Give the position of every Plasmodium parasite.
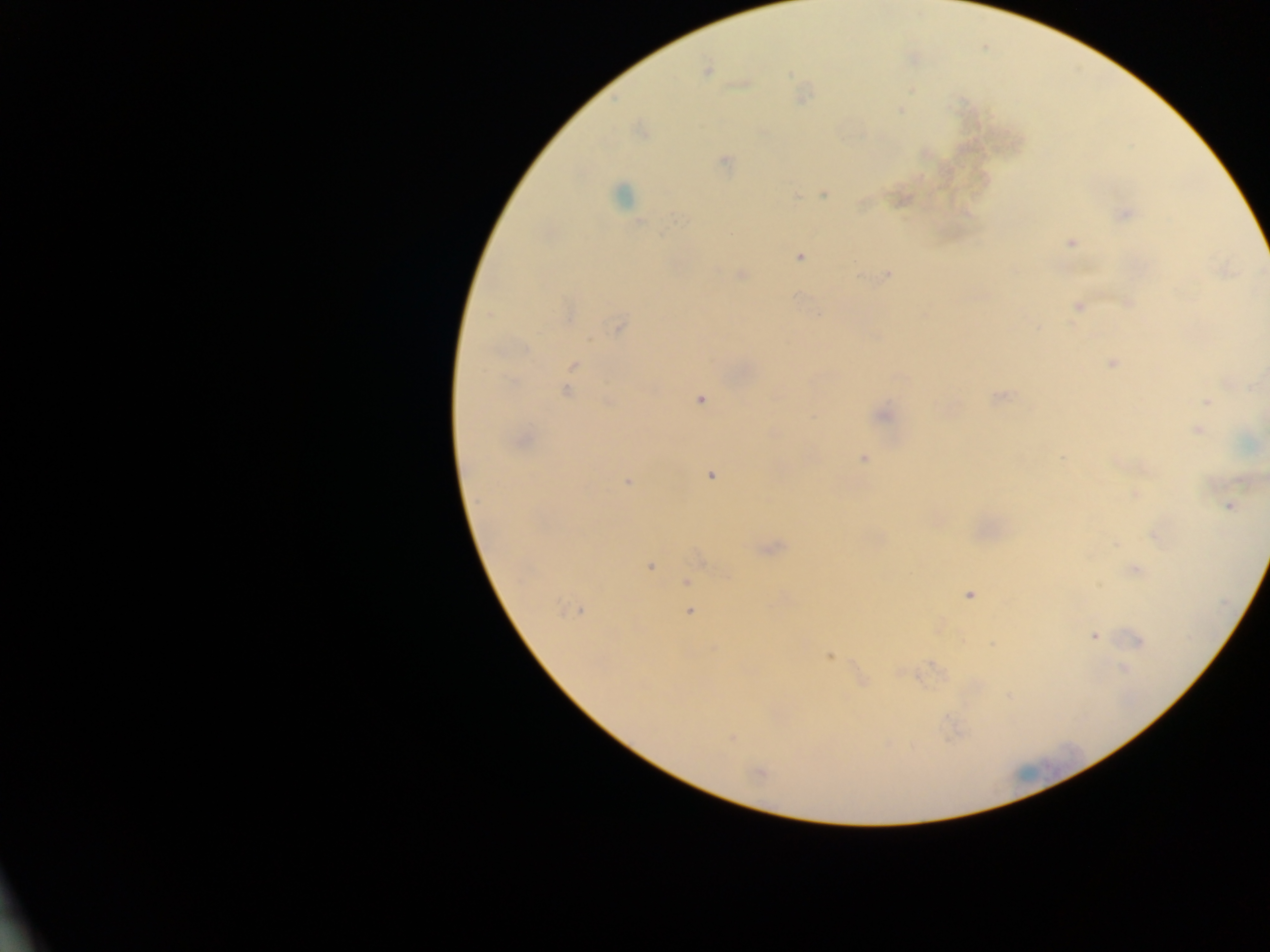

Approximate centers as (x, y) in pixels.
Plasmodium parasites: (706, 71), (789, 73), (900, 111), (639, 131), (725, 160), (621, 194), (824, 194), (796, 196), (1125, 214), (677, 218), (638, 223), (1070, 242), (799, 257), (742, 275), (888, 275), (1128, 303), (1078, 306), (567, 314), (488, 316), (618, 327), (526, 349), (1112, 364), (573, 365), (567, 392), (999, 397), (701, 399), (1207, 402), (884, 415), (1198, 430), (521, 440), (1061, 458), (864, 459), (711, 475), (628, 482), (1135, 494), (1229, 506), (1154, 535), (650, 566), (1136, 571), (687, 582), (969, 595), (576, 610), (689, 612), (1094, 636), (1138, 641), (829, 656), (1123, 668), (732, 739), (758, 772).

Image is 1270×952 pixels. One field of view. Thick blood film. Sample from Ghana. Photographed through a microscope with a mobile-phone camera.